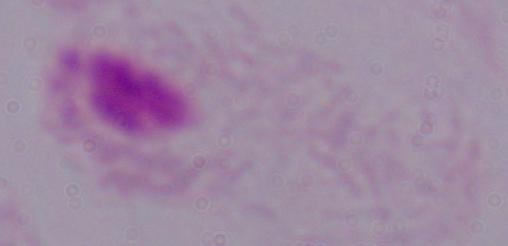

modality = photomicrograph
identification = trichomonad
magnification = 1000x